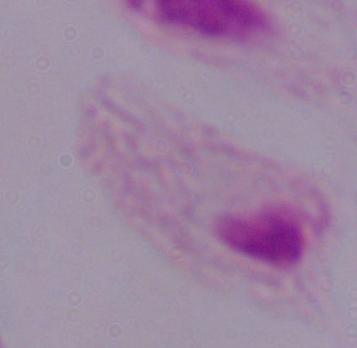

1000x magnification. Micrograph. A trichomonad is shown.